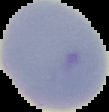
Image is 109×112 pixels. Result: no malaria parasites detected. From a thin blood film. The area outside the segmented cell region is set to black.